Identify the parasite.
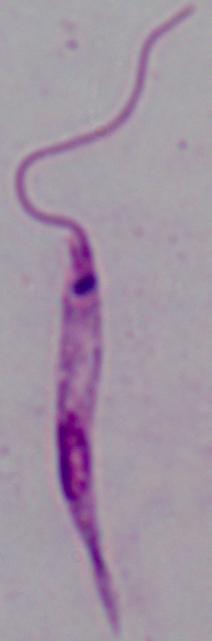

This is Leishmania.

Summary:
  - Magnification: 1000x
  - Modality: photomicrograph